Outline each blood parasite and name the species.
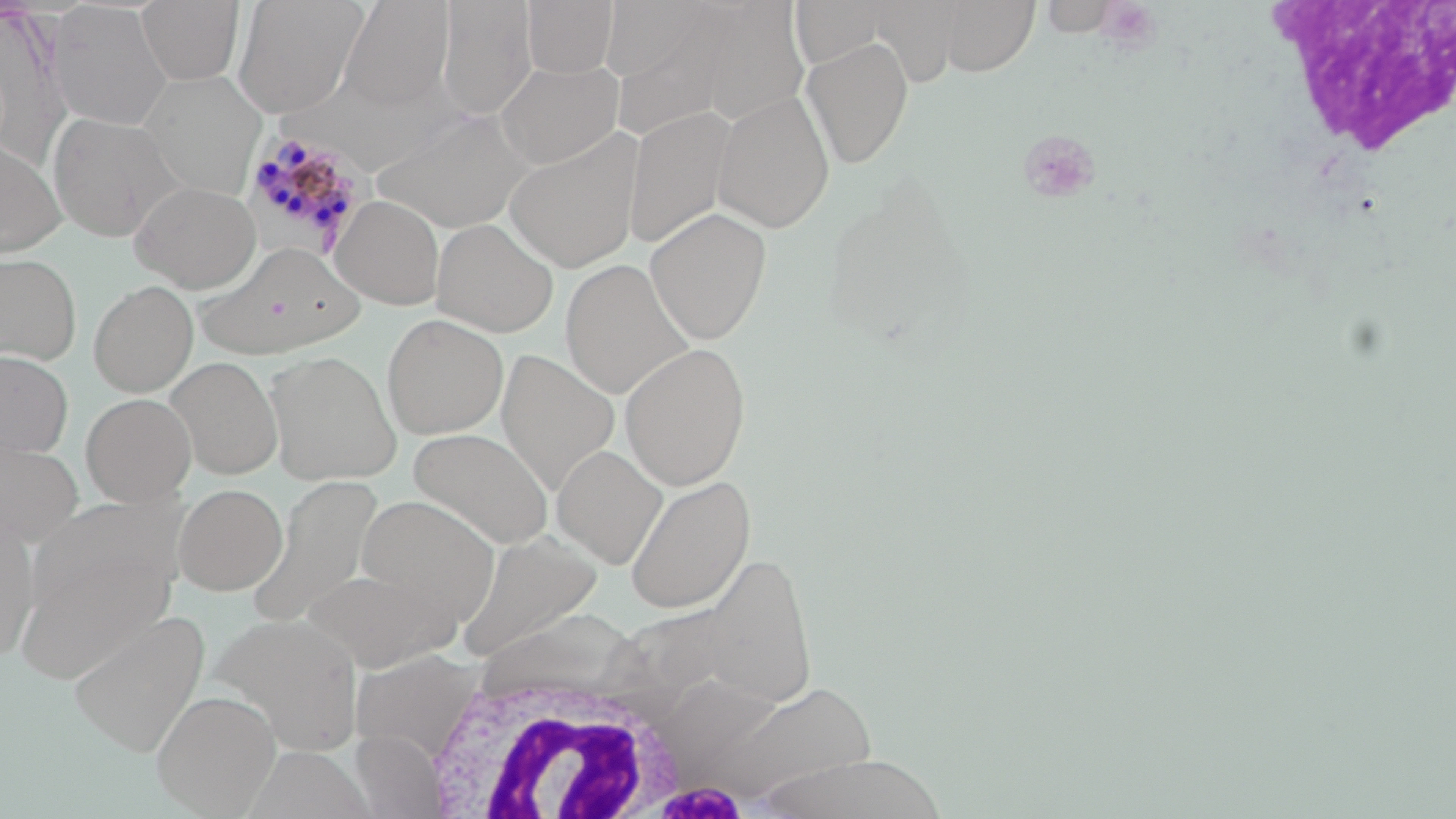

Approximate bounding boxes as (x1, y1, x2, y2) in pixels.
Plasmodium malariae-infected red blood cells: (241, 128, 370, 261).
No Plasmodium falciparum, Plasmodium ovale, Plasmodium vivax, Babesia divergens, or Trypanosoma brucei observed.

Uninfected red blood cell locations: (136, 0, 245, 86), (232, 0, 369, 117), (339, 0, 455, 110), (600, 0, 732, 104), (934, 0, 1039, 76), (434, 1, 537, 121), (522, 1, 619, 79), (790, 1, 893, 72), (860, 1, 966, 86), (1036, 1, 1123, 36), (48, 2, 173, 131), (697, 3, 810, 127), (0, 6, 72, 167), (800, 36, 914, 169), (496, 59, 624, 169), (137, 71, 266, 199), (711, 91, 835, 233), (624, 107, 735, 250), (373, 109, 533, 234), (46, 111, 185, 242), (504, 129, 643, 273), (0, 140, 66, 258), (130, 181, 262, 293), (331, 195, 445, 309), (645, 207, 772, 345), (432, 217, 559, 337), (195, 243, 363, 357), (0, 252, 81, 367), (560, 259, 694, 400), (88, 281, 198, 397), (381, 314, 509, 439), (619, 342, 751, 490), (496, 348, 620, 496), (265, 350, 401, 486), (0, 351, 73, 459), (166, 356, 283, 480), (81, 392, 197, 507), (407, 427, 553, 549), (0, 432, 84, 550), (552, 444, 668, 568), (624, 473, 755, 613), (251, 474, 384, 625), (173, 483, 287, 595), (356, 495, 500, 620), (0, 512, 40, 662), (13, 531, 178, 683), (455, 532, 604, 660), (302, 568, 459, 671), (69, 610, 211, 757), (207, 613, 366, 755), (351, 649, 483, 763), (695, 678, 880, 805), (152, 689, 281, 816), (351, 730, 445, 818), (751, 753, 952, 819). White blood cell locations: (416, 658, 698, 816). Platelet locations: (1096, 2, 1164, 51), (1018, 129, 1102, 205). Slide-level diagnosis: Plasmodium malariae. Image is 1456×819 pixels. Captured at 1000x magnification. One field of a larger specimen. May-Grünwald-Giemsa stain. Thin blood film. Optical microscopy.